Outline each Plasmodium falciparum-infected red blood cell.
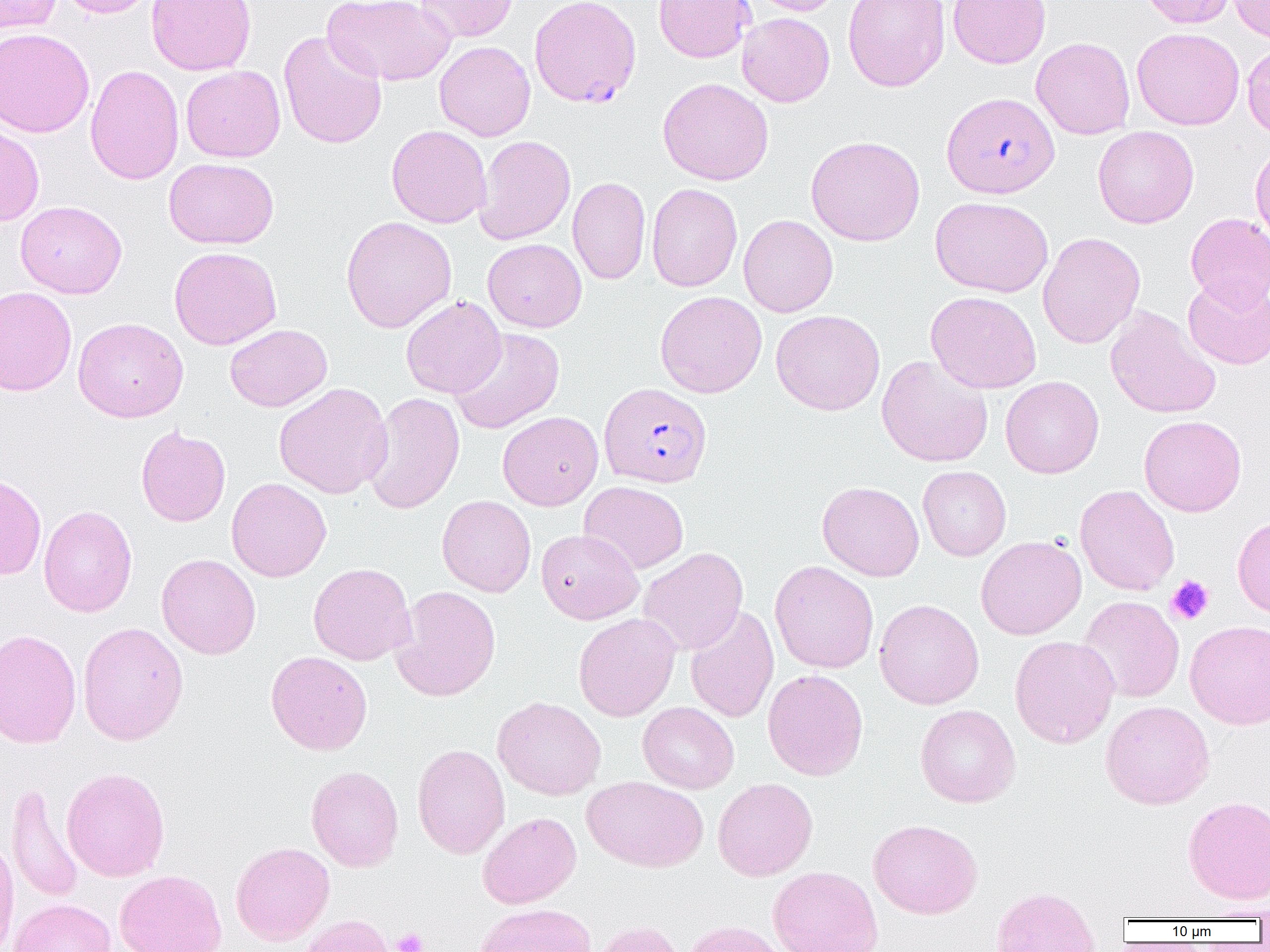

Approximate bounding boxes as named x1/y1/x2/y2 corners in pixels.
Plasmodium falciparum-infected red blood cells: (x1=529, y1=0, x2=641, y2=108), (x1=941, y1=92, x2=1059, y2=198), (x1=599, y1=382, x2=712, y2=488).

slide-level diagnosis = Plasmodium falciparum
preparation = thin blood film
field of view = single
platelet locations = approximate bounding boxes as named x1/y1/x2/y2 corners in pixels: (x1=1166, y1=575, x2=1214, y2=625), (x1=392, y1=928, x2=429, y2=952)
modality = optical microscopy
magnification = 1000x
uninfected red blood cell locations = approximate bounding boxes as named x1/y1/x2/y2 corners in pixels: (x1=0, y1=0, x2=61, y2=34), (x1=55, y1=0, x2=160, y2=18), (x1=146, y1=0, x2=257, y2=76), (x1=323, y1=0, x2=454, y2=86), (x1=415, y1=0, x2=519, y2=43), (x1=654, y1=0, x2=754, y2=62), (x1=746, y1=0, x2=843, y2=16), (x1=843, y1=0, x2=950, y2=92), (x1=948, y1=0, x2=1051, y2=68), (x1=1139, y1=0, x2=1236, y2=28), (x1=1227, y1=1, x2=1270, y2=43), (x1=737, y1=13, x2=835, y2=107), (x1=0, y1=27, x2=94, y2=137), (x1=1132, y1=27, x2=1245, y2=130), (x1=278, y1=31, x2=387, y2=150), (x1=1031, y1=37, x2=1135, y2=140), (x1=434, y1=41, x2=536, y2=141), (x1=1242, y1=43, x2=1270, y2=140), (x1=85, y1=64, x2=184, y2=186), (x1=181, y1=65, x2=285, y2=162), (x1=657, y1=77, x2=774, y2=185), (x1=0, y1=122, x2=45, y2=226), (x1=386, y1=125, x2=491, y2=228), (x1=1092, y1=126, x2=1199, y2=228), (x1=474, y1=135, x2=575, y2=245), (x1=805, y1=135, x2=925, y2=246), (x1=1250, y1=141, x2=1270, y2=247), (x1=163, y1=158, x2=278, y2=249), (x1=567, y1=177, x2=651, y2=285), (x1=646, y1=183, x2=742, y2=292), (x1=930, y1=196, x2=1054, y2=297), (x1=15, y1=200, x2=127, y2=299), (x1=1186, y1=213, x2=1270, y2=311), (x1=738, y1=215, x2=838, y2=317), (x1=340, y1=216, x2=457, y2=333), (x1=1037, y1=232, x2=1145, y2=348), (x1=482, y1=238, x2=586, y2=332), (x1=168, y1=246, x2=282, y2=350), (x1=1182, y1=277, x2=1270, y2=370), (x1=0, y1=286, x2=77, y2=396), (x1=655, y1=291, x2=767, y2=398), (x1=925, y1=291, x2=1042, y2=394), (x1=401, y1=296, x2=506, y2=398), (x1=1105, y1=306, x2=1222, y2=419), (x1=771, y1=309, x2=885, y2=416), (x1=73, y1=317, x2=188, y2=422), (x1=225, y1=324, x2=332, y2=412), (x1=448, y1=327, x2=565, y2=434), (x1=877, y1=355, x2=993, y2=467), (x1=1000, y1=376, x2=1104, y2=479), (x1=273, y1=382, x2=393, y2=499), (x1=363, y1=392, x2=465, y2=514), (x1=498, y1=411, x2=603, y2=510), (x1=1138, y1=415, x2=1247, y2=516), (x1=135, y1=425, x2=231, y2=527), (x1=918, y1=466, x2=1011, y2=561), (x1=0, y1=474, x2=46, y2=581), (x1=226, y1=477, x2=331, y2=582), (x1=579, y1=481, x2=689, y2=574), (x1=817, y1=481, x2=924, y2=581), (x1=1074, y1=484, x2=1180, y2=595), (x1=437, y1=495, x2=536, y2=597), (x1=38, y1=504, x2=137, y2=617), (x1=1232, y1=516, x2=1270, y2=617), (x1=536, y1=529, x2=643, y2=624), (x1=976, y1=536, x2=1087, y2=640), (x1=638, y1=548, x2=748, y2=656), (x1=156, y1=553, x2=261, y2=659), (x1=770, y1=561, x2=879, y2=673), (x1=307, y1=562, x2=417, y2=665), (x1=390, y1=585, x2=501, y2=702), (x1=1078, y1=596, x2=1185, y2=703), (x1=874, y1=598, x2=984, y2=709), (x1=685, y1=604, x2=779, y2=724), (x1=573, y1=613, x2=680, y2=721), (x1=1185, y1=620, x2=1270, y2=729), (x1=77, y1=621, x2=188, y2=746), (x1=0, y1=628, x2=82, y2=748), (x1=1010, y1=635, x2=1120, y2=749), (x1=265, y1=650, x2=373, y2=755), (x1=763, y1=669, x2=868, y2=781), (x1=492, y1=696, x2=606, y2=800), (x1=1100, y1=700, x2=1215, y2=810), (x1=638, y1=702, x2=739, y2=794), (x1=915, y1=704, x2=1020, y2=807), (x1=412, y1=743, x2=510, y2=858), (x1=306, y1=766, x2=404, y2=871), (x1=61, y1=767, x2=170, y2=882), (x1=582, y1=776, x2=708, y2=872), (x1=713, y1=777, x2=818, y2=881), (x1=6, y1=782, x2=85, y2=903), (x1=1183, y1=795, x2=1270, y2=905), (x1=478, y1=812, x2=582, y2=909), (x1=868, y1=818, x2=982, y2=919), (x1=0, y1=836, x2=19, y2=952), (x1=230, y1=841, x2=335, y2=945), (x1=767, y1=866, x2=883, y2=952), (x1=115, y1=870, x2=227, y2=952), (x1=990, y1=885, x2=1100, y2=952), (x1=9, y1=898, x2=116, y2=952), (x1=475, y1=903, x2=597, y2=952), (x1=1196, y1=904, x2=1270, y2=921), (x1=297, y1=915, x2=396, y2=952), (x1=591, y1=920, x2=687, y2=952), (x1=681, y1=920, x2=792, y2=952)
image size = 1270×952 pixels